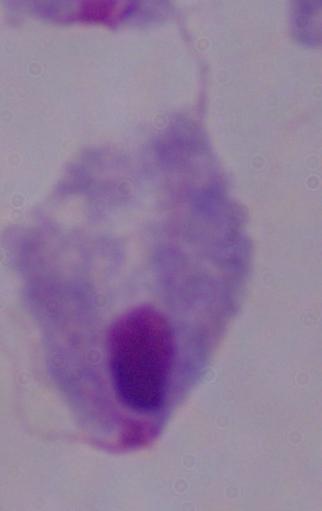
Summary:
  - Magnification: 1000x
  - Identification: trichomonad
  - Modality: micrograph